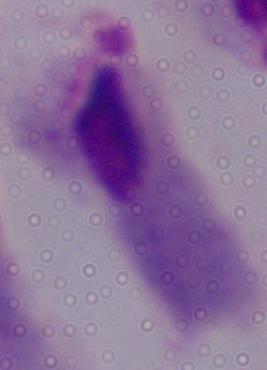

modality = photomicrograph
magnification = 1000x
identification = trichomonad